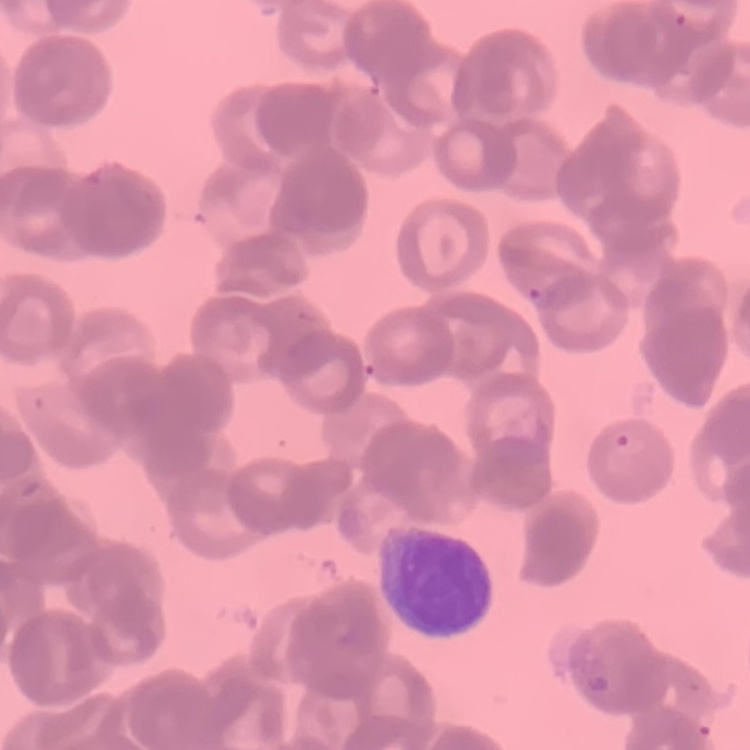

Summary:
  - Erythrocyte morphology: rouleaux formation
  - Image type: one tile cut from a larger photomicrograph
  - Preparation: thin blood film
  - Stain: Field's or Giemsa